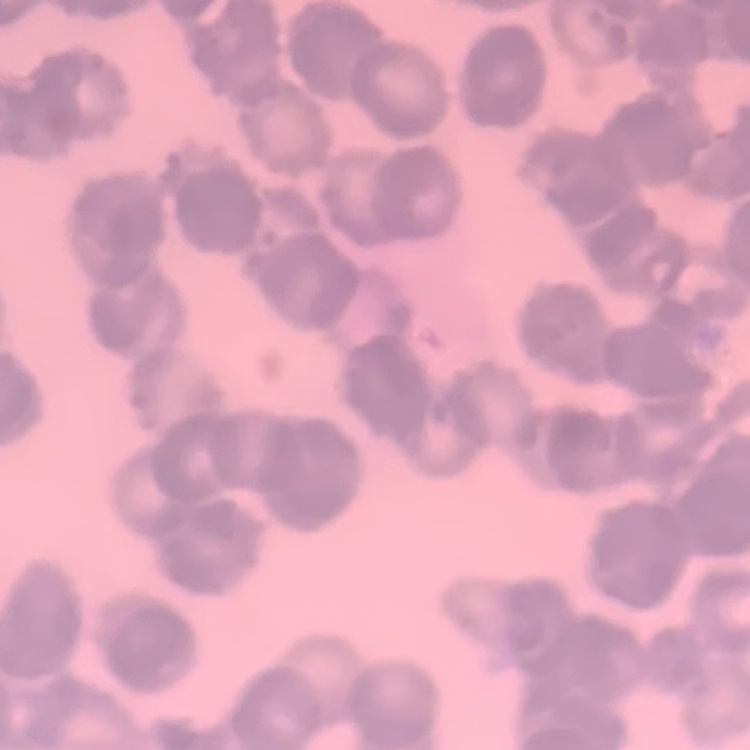
The erythrocytes exhibit rouleaux formation. Stained with either Field's or Giemsa. Thin peripheral smear. One tile cut from a larger photomicrograph.